Describe the morphology of the erythrocytes.
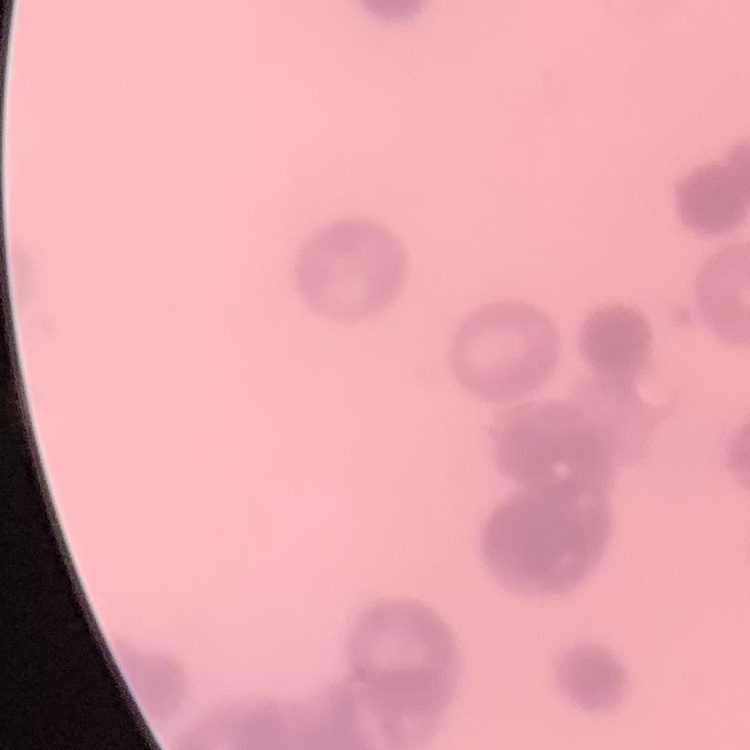
They show rouleaux formation.

Field's or Giemsa stain. Thin blood smear. Square crop of a larger photomicrograph.